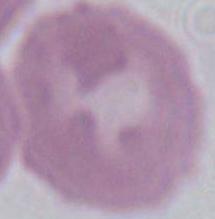
modality: micrograph
identification: red blood cell
magnification: 1000x